Describe the morphology of the erythrocytes.
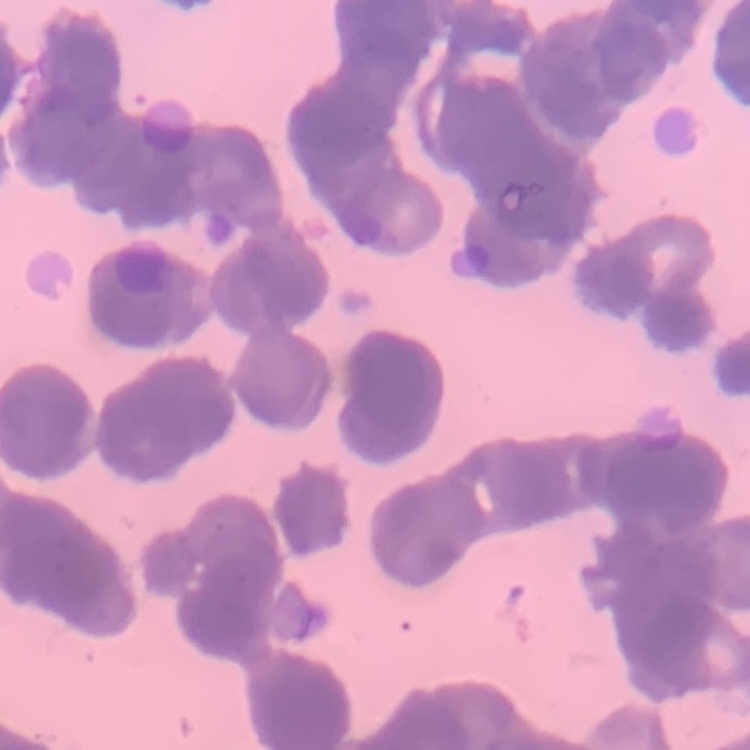
Rouleaux formation.

Summary:
  - Preparation: thin peripheral smear
  - Stain: Field's or Giemsa
  - Image type: one tile cut from a larger photomicrograph